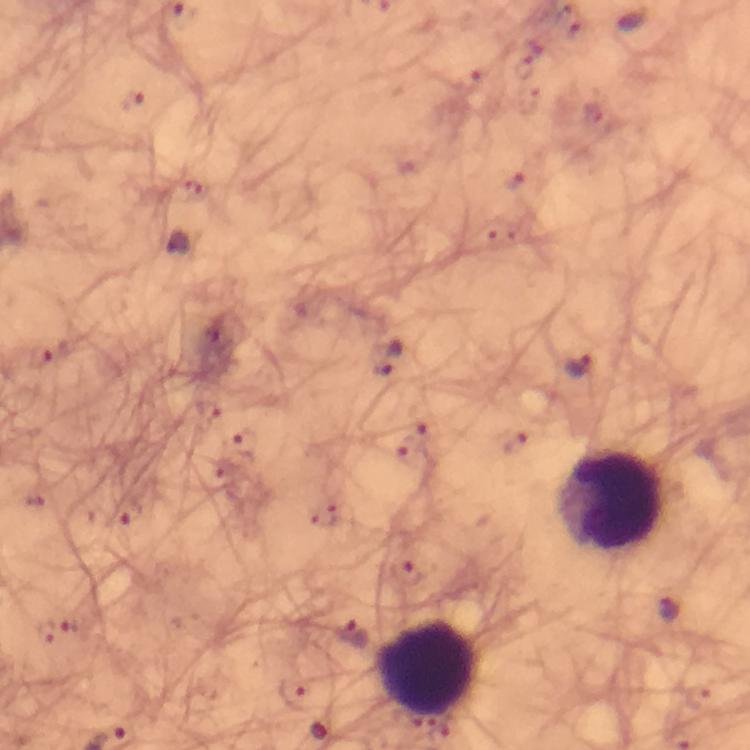

stain = Giemsa
context = from a diagnostic examination for malaria
Plasmodium parasite locations = approximate centers as [x, y] in pixels: [135, 101], [515, 180], [193, 186], [40, 357], [578, 368], [380, 369], [209, 411], [418, 419], [242, 442], [516, 443], [412, 458], [127, 513], [406, 571], [671, 609], [355, 633], [294, 698]
image size = 750×750 pixels
magnification = 100x
immersion oil = applied
cropped from = a single field of view
preparation = thick blood film
leukocyte locations = approximate centers as [x, y] in pixels: [611, 501], [424, 667]
capture = smartphone photograph through a microscope